Assess this cell for malaria.
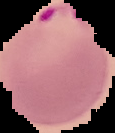
It is parasitized.

{
  "image_size": "115×133 pixels",
  "image_type": "cell region segmented out of the field of view; surrounding area masked to black",
  "preparation": "thin blood film"
}